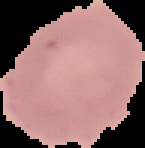

Summary:
  - Image type: segmented cell region on a black background
  - Malaria status: uninfected
  - Preparation: thin blood smear
  - Image size: 145×148 pixels